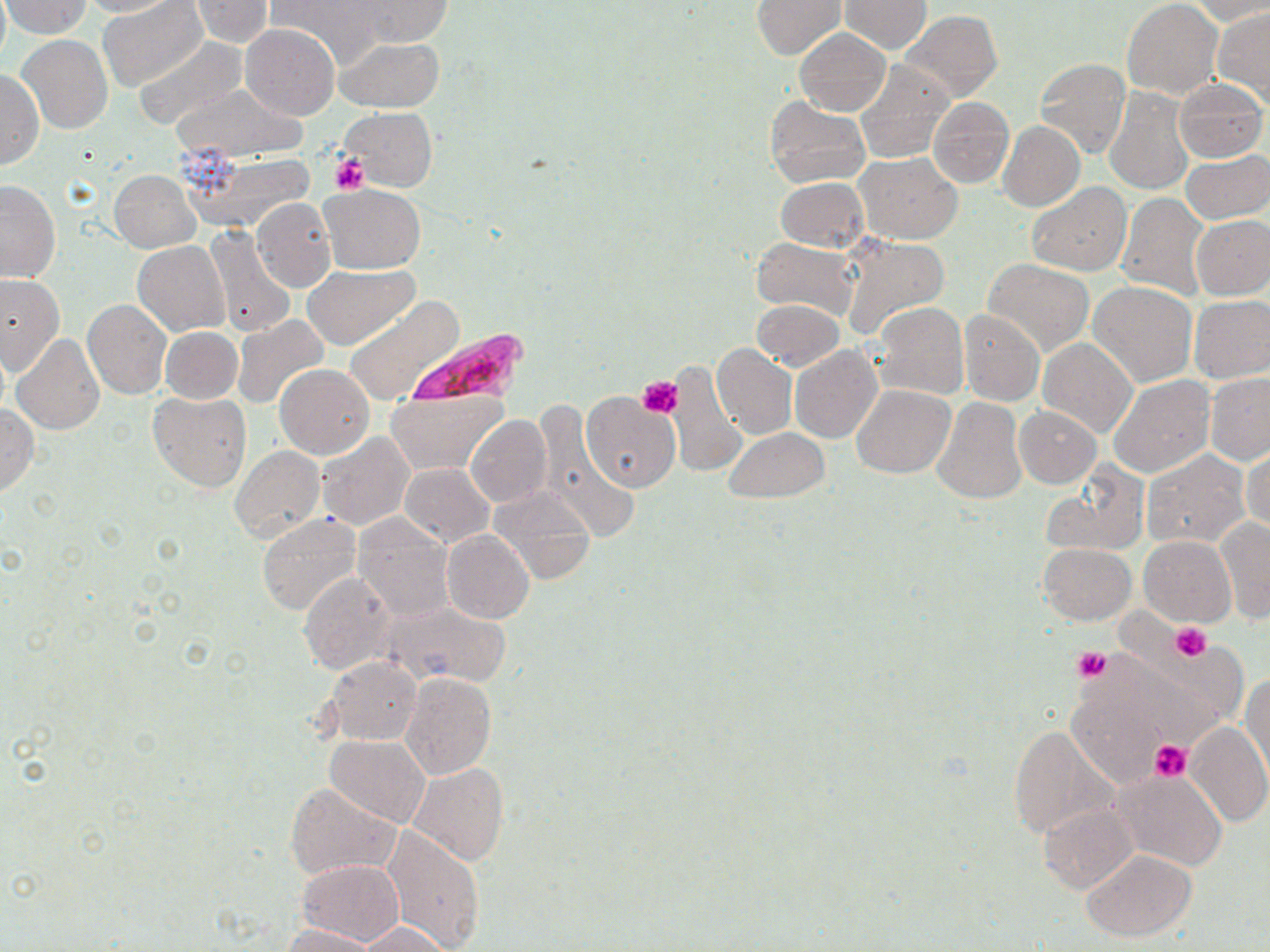
Approximate bounding boxes as named x1/y1/x2/y2 corners in pixels. Platelet locations: (x1=327, y1=152, x2=371, y2=194), (x1=639, y1=376, x2=682, y2=418), (x1=1170, y1=622, x2=1210, y2=660), (x1=1073, y1=646, x2=1111, y2=682), (x1=1150, y1=740, x2=1192, y2=781). Plasmodium falciparum-infected red blood cell locations: (x1=404, y1=325, x2=530, y2=407). Uninfected red blood cell locations: (x1=0, y1=0, x2=11, y2=65), (x1=2, y1=0, x2=91, y2=37), (x1=76, y1=0, x2=179, y2=17), (x1=100, y1=0, x2=206, y2=89), (x1=269, y1=0, x2=387, y2=67), (x1=347, y1=0, x2=452, y2=48), (x1=751, y1=0, x2=845, y2=59), (x1=1121, y1=0, x2=1222, y2=99), (x1=191, y1=1, x2=273, y2=46), (x1=840, y1=1, x2=930, y2=53), (x1=1185, y1=1, x2=1270, y2=25), (x1=1213, y1=5, x2=1270, y2=104), (x1=901, y1=10, x2=1002, y2=102), (x1=240, y1=25, x2=339, y2=121), (x1=795, y1=27, x2=890, y2=116), (x1=19, y1=35, x2=113, y2=134), (x1=134, y1=37, x2=248, y2=129), (x1=335, y1=38, x2=446, y2=112), (x1=1035, y1=57, x2=1131, y2=158), (x1=855, y1=60, x2=954, y2=164), (x1=0, y1=68, x2=43, y2=169), (x1=1172, y1=79, x2=1268, y2=163), (x1=171, y1=83, x2=308, y2=161), (x1=1104, y1=86, x2=1194, y2=193), (x1=765, y1=97, x2=870, y2=189), (x1=928, y1=98, x2=1014, y2=188), (x1=340, y1=107, x2=437, y2=192), (x1=998, y1=121, x2=1085, y2=211), (x1=185, y1=151, x2=317, y2=231), (x1=1181, y1=151, x2=1270, y2=224), (x1=855, y1=153, x2=962, y2=243), (x1=109, y1=170, x2=200, y2=252), (x1=774, y1=177, x2=868, y2=253), (x1=0, y1=180, x2=61, y2=284), (x1=1027, y1=182, x2=1130, y2=276), (x1=320, y1=183, x2=426, y2=273), (x1=1116, y1=193, x2=1208, y2=299), (x1=252, y1=198, x2=336, y2=292), (x1=1191, y1=216, x2=1270, y2=298), (x1=204, y1=225, x2=295, y2=336), (x1=837, y1=234, x2=951, y2=343), (x1=751, y1=237, x2=859, y2=319), (x1=133, y1=242, x2=231, y2=336), (x1=982, y1=259, x2=1093, y2=356), (x1=304, y1=263, x2=417, y2=350), (x1=0, y1=274, x2=66, y2=374), (x1=1089, y1=282, x2=1197, y2=387), (x1=1188, y1=294, x2=1270, y2=383), (x1=345, y1=297, x2=464, y2=406), (x1=81, y1=299, x2=172, y2=399), (x1=751, y1=300, x2=845, y2=370), (x1=871, y1=302, x2=968, y2=400), (x1=958, y1=309, x2=1046, y2=405), (x1=232, y1=315, x2=329, y2=410), (x1=159, y1=326, x2=242, y2=404), (x1=12, y1=335, x2=105, y2=437), (x1=1038, y1=337, x2=1136, y2=438), (x1=712, y1=343, x2=797, y2=440), (x1=790, y1=345, x2=881, y2=443), (x1=669, y1=363, x2=748, y2=477), (x1=275, y1=364, x2=374, y2=458), (x1=1204, y1=373, x2=1270, y2=464), (x1=1109, y1=375, x2=1215, y2=478), (x1=852, y1=384, x2=954, y2=478), (x1=387, y1=389, x2=507, y2=475), (x1=147, y1=391, x2=252, y2=493), (x1=581, y1=392, x2=681, y2=493), (x1=931, y1=398, x2=1027, y2=505), (x1=0, y1=405, x2=39, y2=495), (x1=533, y1=406, x2=638, y2=548), (x1=1015, y1=407, x2=1101, y2=488), (x1=466, y1=414, x2=552, y2=508), (x1=723, y1=428, x2=828, y2=502), (x1=316, y1=432, x2=415, y2=530), (x1=1244, y1=444, x2=1270, y2=537), (x1=230, y1=447, x2=325, y2=544), (x1=1141, y1=449, x2=1250, y2=549), (x1=400, y1=463, x2=495, y2=547), (x1=1041, y1=463, x2=1150, y2=558), (x1=411, y1=465, x2=510, y2=611), (x1=489, y1=485, x2=597, y2=584), (x1=257, y1=513, x2=361, y2=616), (x1=353, y1=515, x2=454, y2=622), (x1=1216, y1=516, x2=1270, y2=624), (x1=443, y1=530, x2=534, y2=623), (x1=1139, y1=534, x2=1235, y2=627), (x1=1038, y1=542, x2=1136, y2=624), (x1=298, y1=571, x2=395, y2=676), (x1=380, y1=599, x2=513, y2=689), (x1=1071, y1=641, x2=1236, y2=769), (x1=325, y1=658, x2=422, y2=745), (x1=402, y1=673, x2=496, y2=779), (x1=1242, y1=674, x2=1270, y2=781), (x1=1184, y1=721, x2=1269, y2=826), (x1=1008, y1=725, x2=1111, y2=841), (x1=325, y1=735, x2=430, y2=829), (x1=406, y1=762, x2=508, y2=865), (x1=1111, y1=769, x2=1230, y2=872), (x1=284, y1=783, x2=401, y2=880), (x1=1040, y1=803, x2=1137, y2=893), (x1=381, y1=823, x2=485, y2=951), (x1=1081, y1=849, x2=1196, y2=941), (x1=294, y1=860, x2=405, y2=946), (x1=354, y1=923, x2=454, y2=952), (x1=281, y1=924, x2=382, y2=951). Slide-level diagnosis: Plasmodium falciparum. Captured at 1000x magnification. One field of a larger specimen. May-Grünwald-Giemsa stain. Optical microscopy. Thin blood smear. Image is 1270×952 pixels.